Find each cell and give its type.
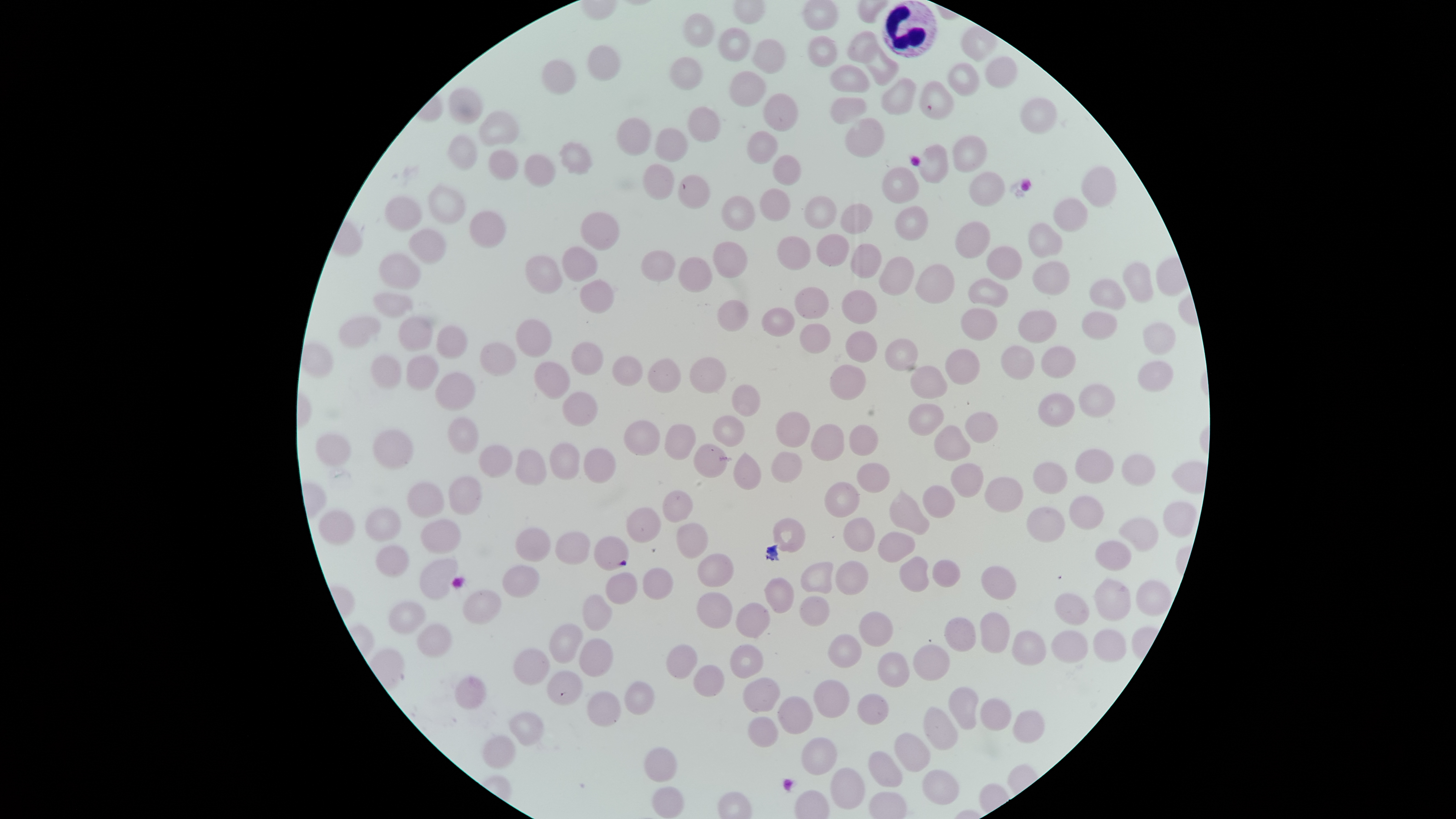
No parasitized red blood cells identified.
Approximate bounding boxes, in pixels from the top-left corner.
Uninfected red blood cells: (left=684, top=12, right=716, bottom=47), (left=719, top=28, right=751, bottom=61), (left=846, top=30, right=877, bottom=63), (left=809, top=35, right=838, bottom=68), (left=752, top=38, right=786, bottom=74), (left=863, top=44, right=900, bottom=85), (left=588, top=45, right=621, bottom=83), (left=985, top=56, right=1018, bottom=89), (left=669, top=57, right=704, bottom=92), (left=542, top=59, right=576, bottom=94), (left=947, top=61, right=980, bottom=97), (left=829, top=65, right=869, bottom=93), (left=730, top=70, right=766, bottom=107), (left=881, top=78, right=917, bottom=116), (left=918, top=81, right=955, bottom=121), (left=448, top=87, right=483, bottom=124), (left=765, top=92, right=799, bottom=130), (left=831, top=97, right=869, bottom=126), (left=1021, top=97, right=1058, bottom=133), (left=688, top=107, right=721, bottom=142), (left=480, top=111, right=519, bottom=145), (left=615, top=118, right=650, bottom=156), (left=844, top=118, right=884, bottom=157), (left=655, top=126, right=688, bottom=163), (left=747, top=131, right=778, bottom=166), (left=449, top=135, right=477, bottom=170), (left=953, top=136, right=988, bottom=172), (left=559, top=141, right=593, bottom=176), (left=918, top=144, right=950, bottom=184), (left=488, top=150, right=518, bottom=178), (left=524, top=154, right=555, bottom=189), (left=772, top=154, right=801, bottom=187), (left=644, top=164, right=673, bottom=199), (left=883, top=166, right=920, bottom=204), (left=1081, top=166, right=1115, bottom=208), (left=971, top=171, right=1007, bottom=208), (left=680, top=175, right=711, bottom=211), (left=429, top=186, right=465, bottom=224), (left=761, top=188, right=791, bottom=220), (left=722, top=195, right=755, bottom=232), (left=804, top=195, right=836, bottom=228), (left=386, top=196, right=422, bottom=231), (left=1053, top=196, right=1088, bottom=233), (left=840, top=204, right=874, bottom=234), (left=895, top=204, right=927, bottom=243), (left=470, top=212, right=506, bottom=248), (left=582, top=212, right=619, bottom=250), (left=955, top=220, right=992, bottom=259), (left=1029, top=221, right=1063, bottom=258), (left=407, top=229, right=447, bottom=265), (left=816, top=234, right=849, bottom=266), (left=777, top=235, right=811, bottom=270), (left=712, top=242, right=747, bottom=277), (left=851, top=244, right=882, bottom=278), (left=987, top=246, right=1022, bottom=280), (left=563, top=247, right=598, bottom=282), (left=642, top=250, right=677, bottom=282), (left=379, top=253, right=419, bottom=289), (left=527, top=256, right=563, bottom=293), (left=679, top=256, right=713, bottom=291), (left=880, top=256, right=915, bottom=295), (left=1032, top=261, right=1070, bottom=294), (left=1124, top=262, right=1154, bottom=306), (left=915, top=264, right=955, bottom=303), (left=969, top=278, right=1008, bottom=308), (left=1091, top=279, right=1126, bottom=310), (left=580, top=280, right=614, bottom=314), (left=794, top=286, right=829, bottom=319), (left=842, top=290, right=878, bottom=323), (left=375, top=292, right=412, bottom=317), (left=717, top=300, right=748, bottom=332), (left=762, top=306, right=794, bottom=337), (left=961, top=310, right=998, bottom=341), (left=1018, top=311, right=1057, bottom=342), (left=1082, top=311, right=1117, bottom=340), (left=340, top=316, right=380, bottom=348), (left=398, top=317, right=431, bottom=351), (left=516, top=319, right=552, bottom=356), (left=1142, top=322, right=1177, bottom=356), (left=801, top=323, right=830, bottom=353), (left=436, top=326, right=468, bottom=358), (left=846, top=330, right=877, bottom=363), (left=883, top=338, right=919, bottom=373), (left=571, top=342, right=603, bottom=377), (left=480, top=343, right=518, bottom=376), (left=1001, top=346, right=1035, bottom=381), (left=1043, top=346, right=1075, bottom=378), (left=945, top=348, right=981, bottom=384), (left=406, top=354, right=439, bottom=392), (left=372, top=356, right=401, bottom=389), (left=613, top=356, right=644, bottom=385), (left=689, top=357, right=725, bottom=394), (left=647, top=359, right=681, bottom=392), (left=1137, top=359, right=1174, bottom=392), (left=535, top=360, right=570, bottom=400), (left=828, top=364, right=868, bottom=400), (left=910, top=366, right=948, bottom=400), (left=436, top=372, right=476, bottom=411), (left=731, top=383, right=761, bottom=417), (left=1079, top=383, right=1114, bottom=419), (left=563, top=392, right=597, bottom=426), (left=1037, top=392, right=1075, bottom=427), (left=908, top=403, right=945, bottom=435), (left=965, top=411, right=998, bottom=444), (left=777, top=412, right=810, bottom=448), (left=713, top=415, right=745, bottom=446), (left=448, top=417, right=479, bottom=454), (left=623, top=420, right=661, bottom=455), (left=811, top=423, right=844, bottom=461), (left=664, top=424, right=695, bottom=460), (left=849, top=424, right=879, bottom=456), (left=934, top=425, right=972, bottom=461), (left=373, top=428, right=413, bottom=470), (left=316, top=433, right=353, bottom=467), (left=550, top=443, right=580, bottom=480), (left=695, top=444, right=728, bottom=479), (left=479, top=445, right=512, bottom=478), (left=585, top=449, right=616, bottom=483), (left=1074, top=449, right=1115, bottom=484), (left=515, top=450, right=548, bottom=486), (left=771, top=451, right=804, bottom=485), (left=733, top=452, right=763, bottom=491), (left=1122, top=453, right=1155, bottom=486), (left=1032, top=462, right=1068, bottom=495), (left=858, top=463, right=891, bottom=494), (left=950, top=463, right=984, bottom=496), (left=448, top=475, right=482, bottom=515), (left=985, top=476, right=1024, bottom=513), (left=823, top=482, right=860, bottom=518), (left=408, top=483, right=444, bottom=517), (left=924, top=485, right=955, bottom=517), (left=889, top=488, right=930, bottom=536), (left=664, top=489, right=694, bottom=522), (left=1069, top=495, right=1104, bottom=530), (left=1164, top=500, right=1197, bottom=538), (left=1028, top=506, right=1066, bottom=543), (left=627, top=507, right=662, bottom=544), (left=365, top=508, right=400, bottom=543), (left=317, top=511, right=355, bottom=545), (left=1119, top=517, right=1160, bottom=551), (left=844, top=518, right=875, bottom=554), (left=419, top=519, right=462, bottom=553), (left=773, top=519, right=806, bottom=553), (left=677, top=523, right=709, bottom=560), (left=516, top=528, right=551, bottom=564), (left=556, top=531, right=591, bottom=565), (left=878, top=531, right=915, bottom=562), (left=595, top=536, right=629, bottom=571), (left=1096, top=541, right=1132, bottom=571), (left=376, top=546, right=409, bottom=578), (left=696, top=553, right=736, bottom=587), (left=900, top=556, right=929, bottom=593), (left=420, top=559, right=459, bottom=602), (left=837, top=560, right=869, bottom=597), (left=932, top=560, right=961, bottom=587), (left=801, top=561, right=834, bottom=594), (left=502, top=565, right=540, bottom=598), (left=981, top=565, right=1017, bottom=601), (left=642, top=568, right=673, bottom=601), (left=607, top=572, right=639, bottom=604), (left=765, top=577, right=795, bottom=614), (left=1095, top=578, right=1132, bottom=623), (left=1136, top=580, right=1171, bottom=616), (left=463, top=590, right=502, bottom=624), (left=697, top=591, right=733, bottom=628), (left=1055, top=593, right=1089, bottom=626), (left=583, top=594, right=612, bottom=631), (left=801, top=596, right=830, bottom=627), (left=388, top=600, right=426, bottom=637), (left=736, top=603, right=771, bottom=637), (left=858, top=612, right=894, bottom=647), (left=980, top=612, right=1010, bottom=654), (left=945, top=617, right=976, bottom=652), (left=417, top=622, right=454, bottom=658), (left=548, top=623, right=582, bottom=663), (left=1093, top=628, right=1127, bottom=661), (left=1012, top=631, right=1045, bottom=665), (left=1052, top=631, right=1088, bottom=663), (left=829, top=634, right=861, bottom=667), (left=580, top=639, right=614, bottom=678), (left=665, top=644, right=697, bottom=679), (left=913, top=644, right=951, bottom=681), (left=730, top=645, right=765, bottom=679), (left=513, top=648, right=550, bottom=684), (left=878, top=652, right=910, bottom=688), (left=694, top=664, right=725, bottom=697), (left=548, top=670, right=583, bottom=707), (left=454, top=676, right=486, bottom=710), (left=741, top=678, right=780, bottom=712), (left=814, top=680, right=849, bottom=719), (left=625, top=681, right=654, bottom=716), (left=948, top=686, right=980, bottom=730), (left=588, top=691, right=622, bottom=727), (left=856, top=693, right=888, bottom=726), (left=778, top=696, right=812, bottom=734), (left=981, top=698, right=1011, bottom=731), (left=924, top=706, right=958, bottom=751), (left=1014, top=710, right=1043, bottom=744), (left=506, top=712, right=542, bottom=747), (left=747, top=717, right=779, bottom=748), (left=481, top=733, right=515, bottom=769), (left=893, top=733, right=931, bottom=771), (left=801, top=736, right=836, bottom=776), (left=643, top=747, right=677, bottom=782), (left=868, top=750, right=901, bottom=788), (left=831, top=768, right=865, bottom=811), (left=923, top=769, right=959, bottom=805), (left=652, top=787, right=683, bottom=819).
White blood cells: (left=882, top=1, right=937, bottom=57).

Summary:
  - Preparation: thin smear of blood
  - Capture: smartphone photograph through the microscope eyepiece
  - Image size: 1456×819 pixels
  - Stain: Giemsa
  - Visible region: circular
  - Field of view: single